Evaluate for parasitized red blood cells.
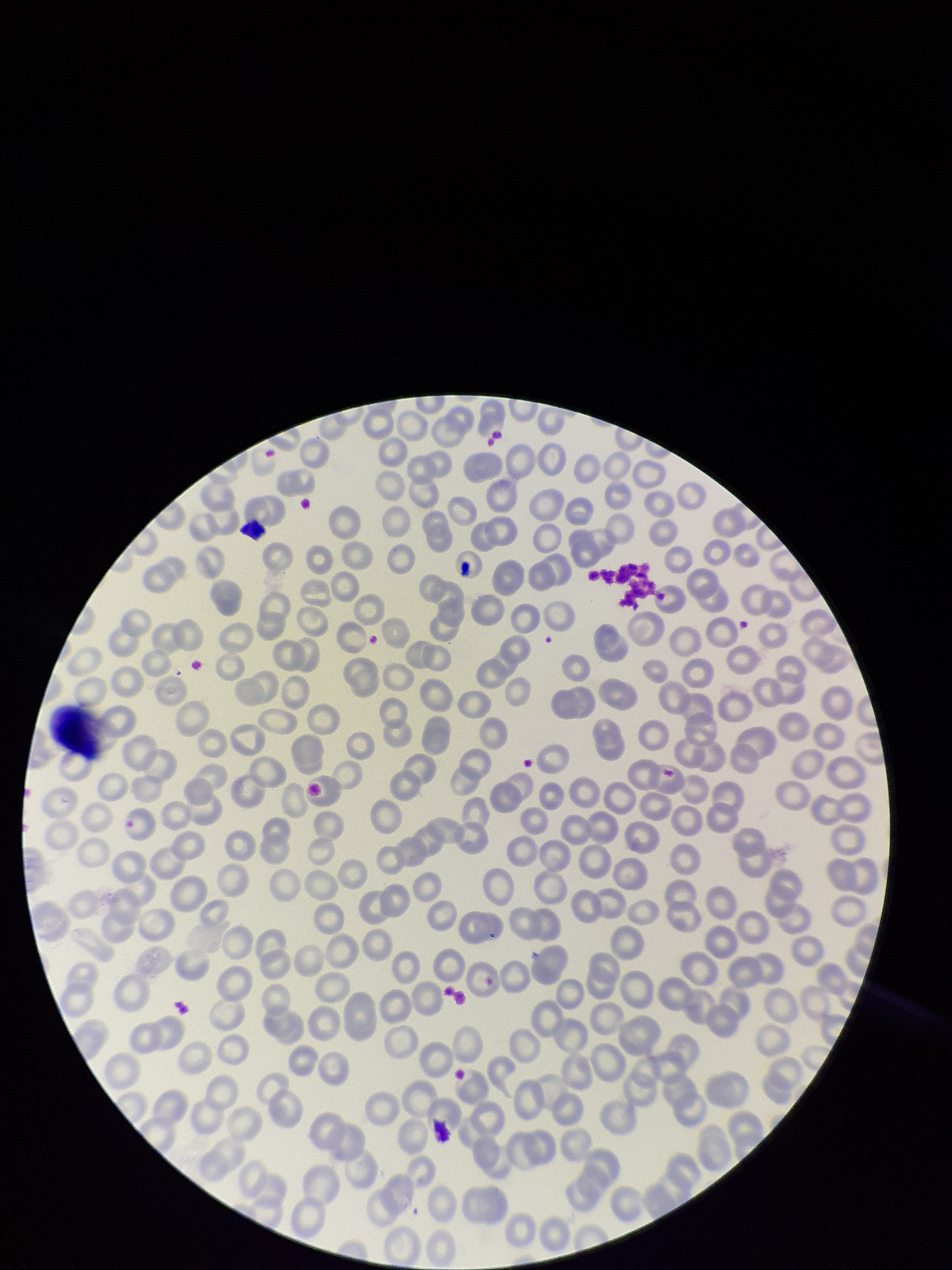

None identified.

Red blood cell count: 228. Patient malaria status: negative. Preparation: thin smear. Image is 952×1270 pixels. Stained with Giemsa. Single field of view. Parasitized red blood cell count: 0. Smartphone photograph taken through the eyepiece of a microscope.